Point out each Plasmodium parasite and each leukocyte.
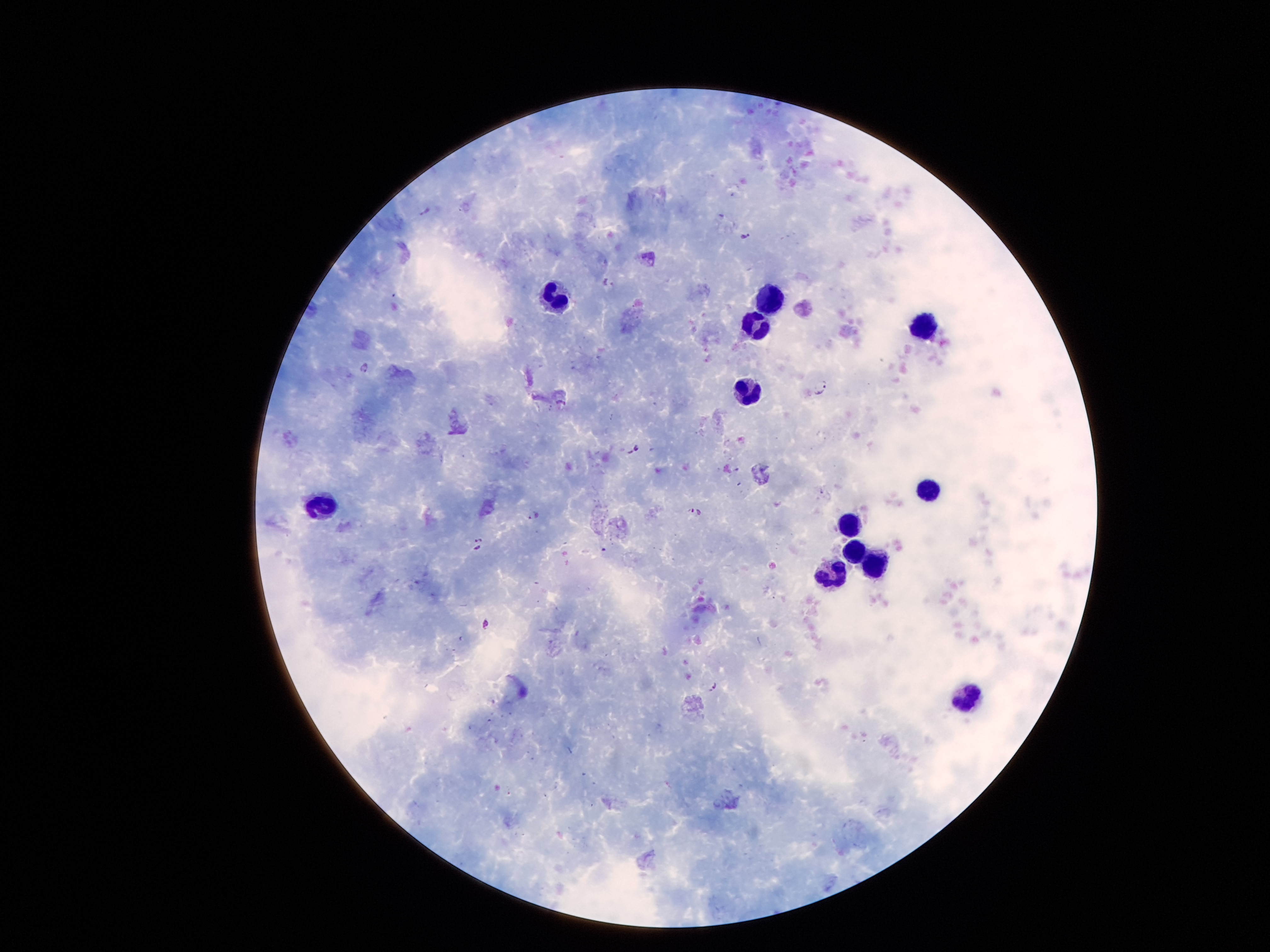

Approximate centers as (x, y) in pixels.
Plasmodium parasites: (425, 212), (745, 236), (608, 285), (364, 367), (822, 386), (636, 449), (695, 510), (534, 516), (479, 545), (486, 623), (711, 686).
Leukocytes: (556, 298), (772, 302), (923, 326), (755, 330), (745, 388), (929, 491), (321, 505), (852, 526), (852, 552), (870, 562), (830, 578), (969, 697).

Summary:
  - Field of view: single
  - Magnification: 100x
  - Preparation: thick peripheral-blood smear
  - Capture: smartphone through the microscope eyepiece
  - Stain: Giemsa
  - Patient malaria status: infected with Plasmodium falciparum
  - Image size: 1270×952 pixels